Describe the morphology of the red blood cells.
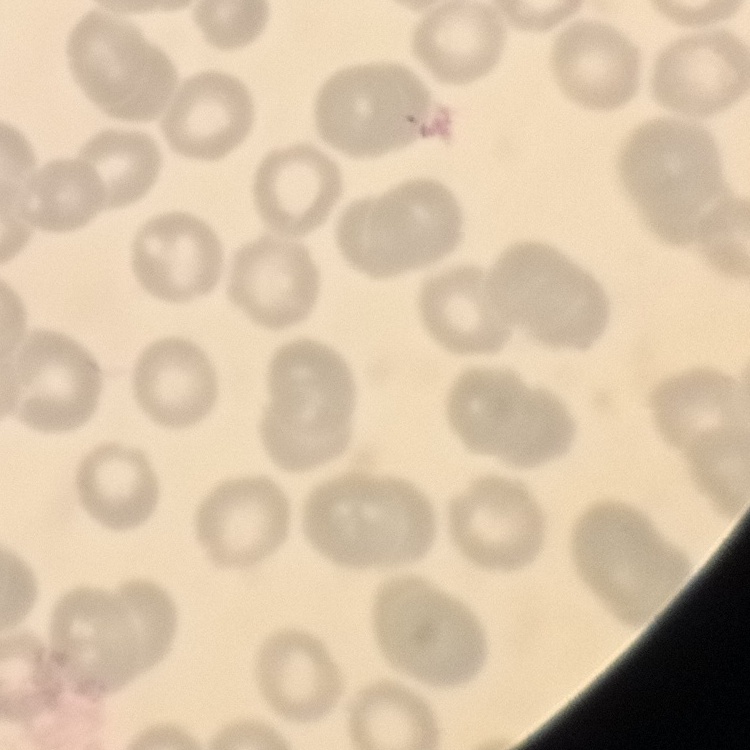

No rouleaux formation.

Summary:
  - Preparation: thin blood film
  - Image type: square crop of a larger photomicrograph
  - Stain: Field's or Giemsa